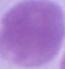 An erythrocyte is shown. Micrograph. Captured at 1000x magnification.